Point out each malaria parasite and classify it by life-cycle stage.
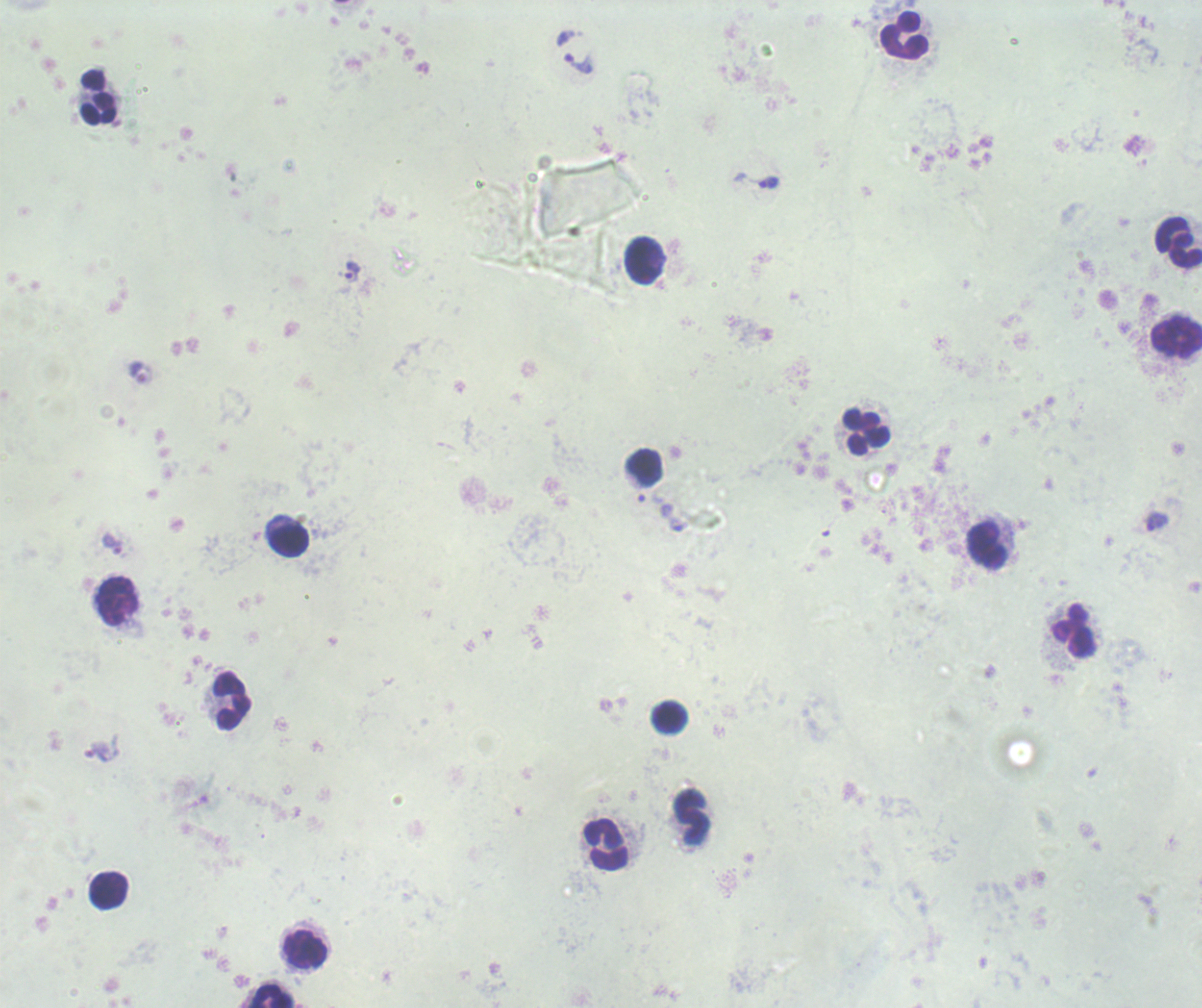
Approximate centers as (x, y) in pixels.
Trophozoites: (578, 63), (770, 182), (352, 271), (1157, 522), (678, 524), (112, 544).
No schizont or gametocyte forms observed.

coordinate format = approximate centers as (x, y) in pixels
leukocyte locations = (905, 36), (98, 97), (1178, 242), (644, 260), (1176, 336), (867, 433), (645, 466), (291, 542), (986, 545), (118, 602), (1072, 631), (232, 700), (670, 717), (693, 817), (606, 844), (109, 891), (306, 950), (272, 995)
preparation = thick blood film
image size = 1202×1008 pixels
background quality = unsatisfactory
magnification = 100x
field of view = one from this slide
context = previously used in a real diagnosis
stain = Romanowsky